Name the parasite shown.
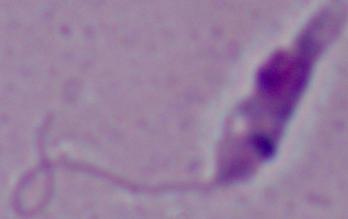
This is Leishmania.

1000x magnification. Micrograph.